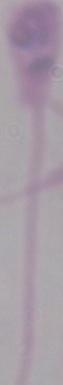
Micrograph. 1000x magnification. A Leishmania parasite is seen.